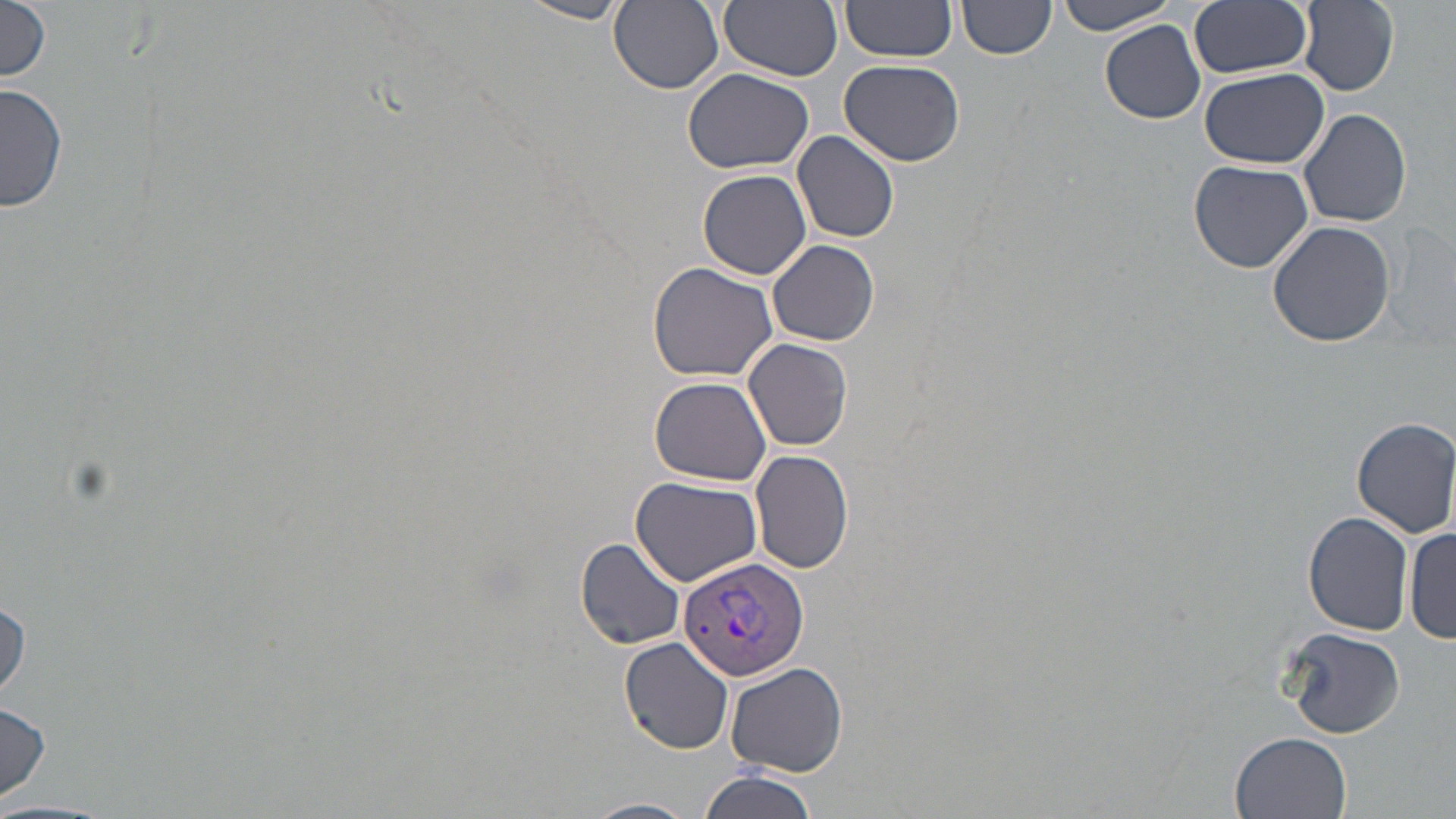

slide-level diagnosis = Plasmodium vivax
stain = May-Grünwald-Giemsa
uninfected red blood cell locations = approximate bounding boxes as (x1, y1, x2, y2) in pixels: (518, 0, 631, 24), (609, 0, 723, 94), (720, 0, 843, 79), (841, 0, 958, 61), (1190, 0, 1312, 79), (1052, 1, 1187, 35), (1292, 1, 1399, 97), (1, 2, 52, 83), (957, 2, 1056, 62), (1101, 21, 1205, 124), (839, 59, 965, 166), (683, 67, 814, 173), (1199, 67, 1329, 169), (1, 84, 69, 214), (1299, 107, 1413, 228), (792, 130, 899, 243), (1188, 160, 1313, 275), (698, 169, 812, 279), (1267, 220, 1397, 348), (768, 240, 880, 346), (647, 262, 778, 382), (744, 339, 853, 452), (650, 376, 771, 485), (1351, 417, 1456, 537), (750, 449, 854, 574), (631, 475, 764, 585), (1302, 512, 1414, 636), (1405, 523, 1455, 640), (575, 537, 686, 650), (0, 596, 28, 700), (1280, 626, 1406, 741), (620, 639, 735, 754), (726, 661, 848, 776), (0, 702, 52, 804), (1231, 731, 1351, 818), (699, 769, 819, 819), (584, 798, 698, 819)
image size = 1456×819 pixels
magnification = 1000x
preparation = thin blood smear
Plasmodium vivax-infected red blood cell locations = approximate bounding boxes as (x1, y1, x2, y2) in pixels: (678, 555, 809, 682)
modality = optical microscopy
field of view = single